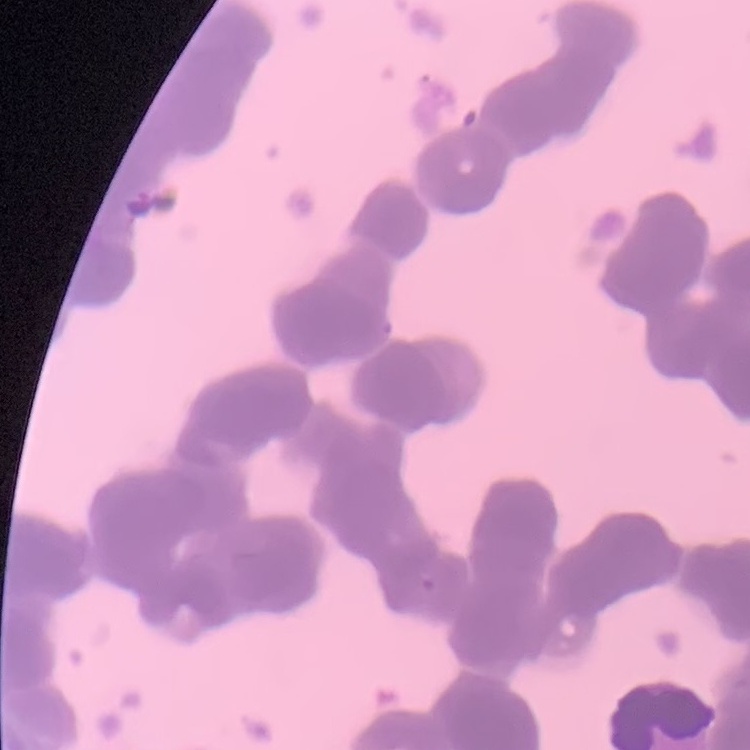

Summary:
  - Erythrocyte morphology: rouleaux formation
  - Stain: Field's or Giemsa
  - Image type: one tile cut from a larger photomicrograph
  - Preparation: thin blood film